Comment on the morphology of the erythrocytes.
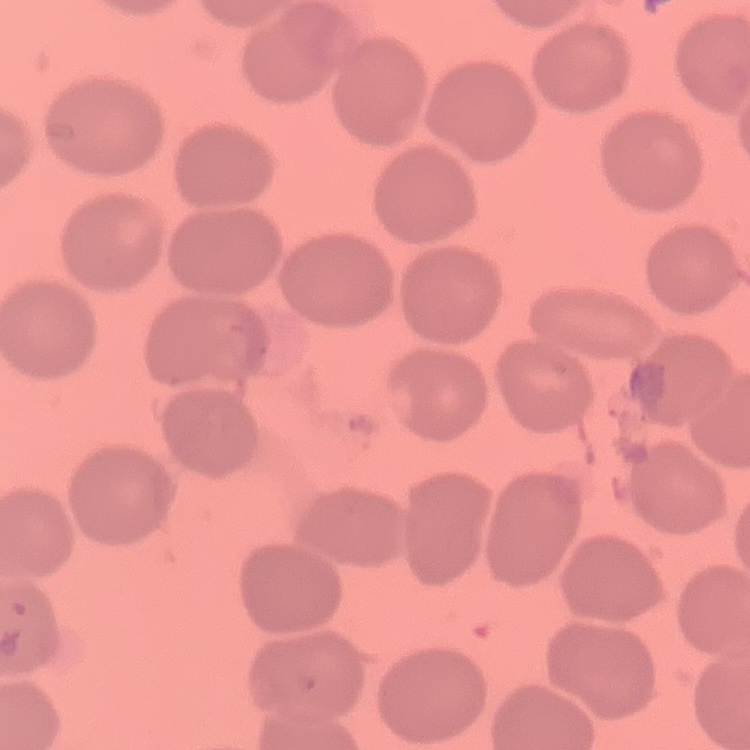

No rouleaux formation.

{
  "preparation": "thin peripheral smear",
  "image_type": "one tile cut from a larger photomicrograph",
  "stain": "Field's or Giemsa"
}